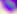

Summary:
  - Modality: photomicrograph
  - Identification: Toxoplasma gondii
  - Magnification: 400x